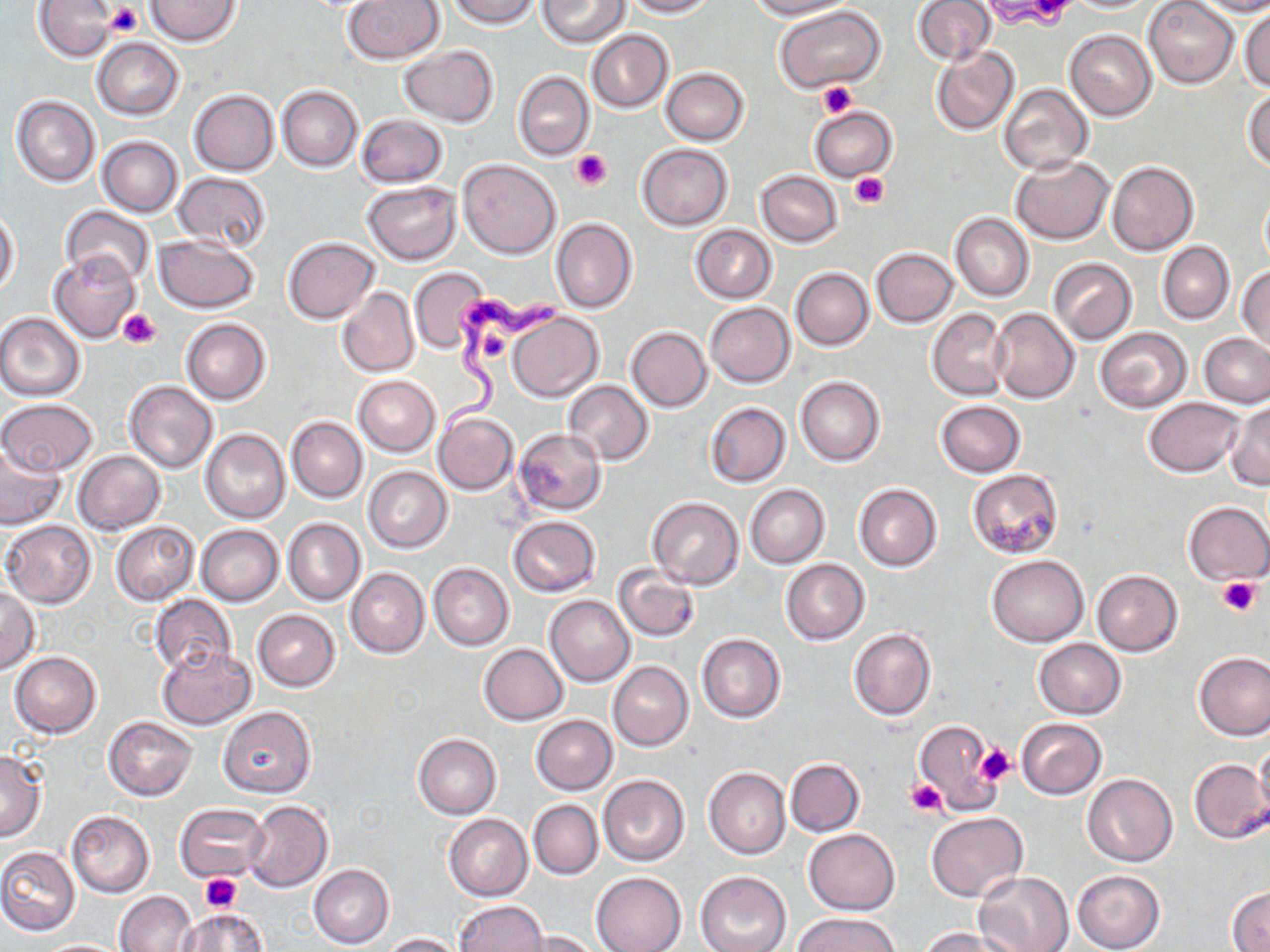
Approximate bounding boxes as [x1, y1, x2, y2] in pixels. Trypanosoma brucei locations: [440, 294, 568, 437]. Uninfected red blood cell locations: [35, 0, 118, 61], [146, 0, 243, 45], [343, 0, 445, 64], [447, 0, 540, 29], [537, 0, 630, 47], [624, 0, 714, 17], [747, 0, 853, 20], [911, 0, 995, 66], [982, 0, 1067, 24], [1143, 0, 1239, 88], [1190, 0, 1270, 16], [775, 6, 886, 93], [1240, 7, 1269, 91], [584, 29, 674, 113], [1064, 29, 1156, 121], [92, 37, 184, 119], [398, 45, 499, 127], [931, 45, 1019, 135], [661, 68, 749, 145], [513, 71, 593, 160], [997, 84, 1093, 175], [277, 85, 362, 170], [187, 89, 279, 175], [1244, 89, 1270, 172], [11, 95, 100, 188], [809, 107, 897, 182], [355, 114, 448, 189], [98, 136, 184, 217], [637, 143, 733, 230], [1010, 156, 1114, 245], [458, 159, 560, 258], [1106, 161, 1198, 256], [756, 170, 842, 248], [173, 172, 271, 252], [364, 181, 461, 263], [1260, 190, 1270, 271], [59, 205, 155, 287], [0, 210, 20, 294], [950, 212, 1034, 303], [550, 218, 639, 314], [690, 225, 777, 303], [153, 236, 261, 313], [282, 237, 379, 324], [1158, 241, 1235, 324], [871, 248, 958, 327], [49, 252, 140, 343], [1046, 258, 1137, 344], [1237, 264, 1270, 354], [408, 267, 488, 352], [790, 267, 875, 350], [337, 286, 419, 377], [705, 302, 795, 388], [927, 308, 1012, 400], [990, 308, 1080, 402], [0, 312, 86, 401], [507, 313, 603, 402], [181, 318, 270, 404], [624, 320, 791, 404], [627, 327, 712, 412], [1095, 327, 1191, 412], [1199, 333, 1270, 408], [353, 375, 439, 456], [795, 376, 884, 466], [563, 379, 653, 465], [123, 380, 217, 473], [1142, 397, 1245, 478], [0, 399, 99, 477], [935, 400, 1026, 477], [1225, 401, 1269, 490], [705, 402, 791, 487], [433, 412, 518, 495], [286, 416, 367, 502], [201, 428, 290, 524], [513, 428, 606, 516], [0, 442, 69, 532], [72, 450, 165, 535], [364, 467, 453, 552], [967, 468, 1064, 560], [745, 484, 830, 569], [853, 484, 941, 572], [646, 498, 743, 589], [1183, 501, 1270, 584], [508, 516, 600, 597], [284, 518, 365, 604], [2, 519, 97, 608], [111, 521, 199, 605], [196, 525, 284, 606], [988, 555, 1088, 646], [781, 558, 869, 644], [428, 563, 514, 651], [613, 565, 701, 642], [346, 567, 429, 658], [1091, 570, 1184, 656], [0, 584, 41, 674], [545, 594, 636, 686], [149, 595, 235, 675], [252, 609, 341, 691], [849, 627, 936, 721], [696, 634, 786, 723], [1034, 638, 1126, 719], [479, 643, 568, 724], [156, 645, 254, 729], [10, 651, 102, 737], [1194, 652, 1270, 739], [608, 661, 693, 751], [218, 706, 315, 798], [532, 715, 617, 795], [103, 716, 197, 800], [915, 717, 1002, 812], [1014, 717, 1106, 799], [413, 732, 501, 819], [1255, 739, 1270, 821], [0, 750, 47, 840], [784, 758, 864, 836], [1187, 758, 1268, 844], [704, 767, 790, 859], [599, 774, 689, 867], [1082, 774, 1178, 867], [529, 799, 603, 879], [243, 800, 334, 892], [175, 803, 269, 882], [66, 811, 154, 897], [927, 812, 1027, 902], [442, 813, 533, 901], [803, 828, 900, 915], [0, 847, 80, 935], [309, 864, 394, 948], [1071, 869, 1166, 952], [694, 871, 790, 952], [975, 871, 1075, 952], [592, 872, 686, 952], [1227, 886, 1270, 950], [115, 891, 196, 952], [454, 901, 548, 952], [176, 906, 270, 951], [795, 912, 902, 952], [917, 927, 1013, 952], [521, 930, 603, 952], [381, 932, 461, 951]. Platelet locations: [1026, 0, 1075, 23], [104, 1, 144, 36], [988, 1, 1071, 28], [816, 81, 857, 118], [570, 149, 612, 190], [850, 172, 888, 208], [116, 308, 162, 350], [480, 332, 514, 363], [1218, 578, 1261, 615], [976, 743, 1015, 785], [906, 779, 948, 817], [201, 873, 243, 911]. Slide-level diagnosis: Trypanosoma brucei. Single field of view. Image is 1270×952 pixels. Light microscopy. Thin blood film. 1000x magnification. May-Grünwald-Giemsa-stained preparation.